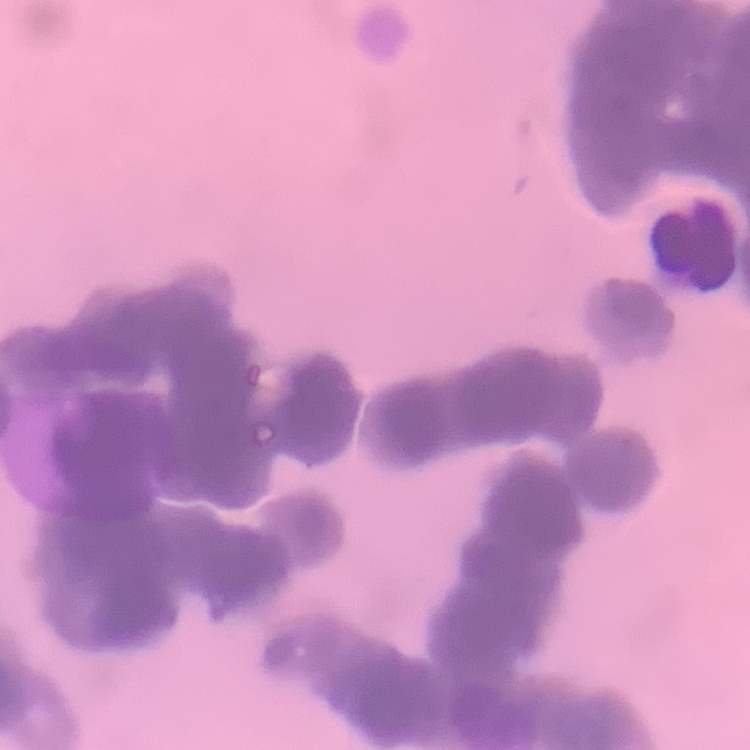

erythrocyte morphology = rouleaux formation
preparation = thin peripheral smear
image type = one tile cut from a larger photomicrograph
stain = Field's or Giemsa